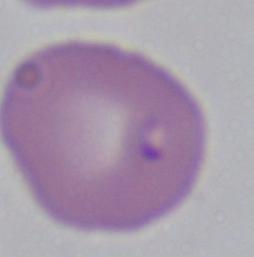

modality = photomicrograph
identification = Babesia
magnification = 1000x